Name the parasite shown.
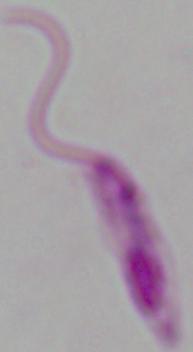

This is Leishmania.

Summary:
  - Modality: micrograph
  - Magnification: 1000x